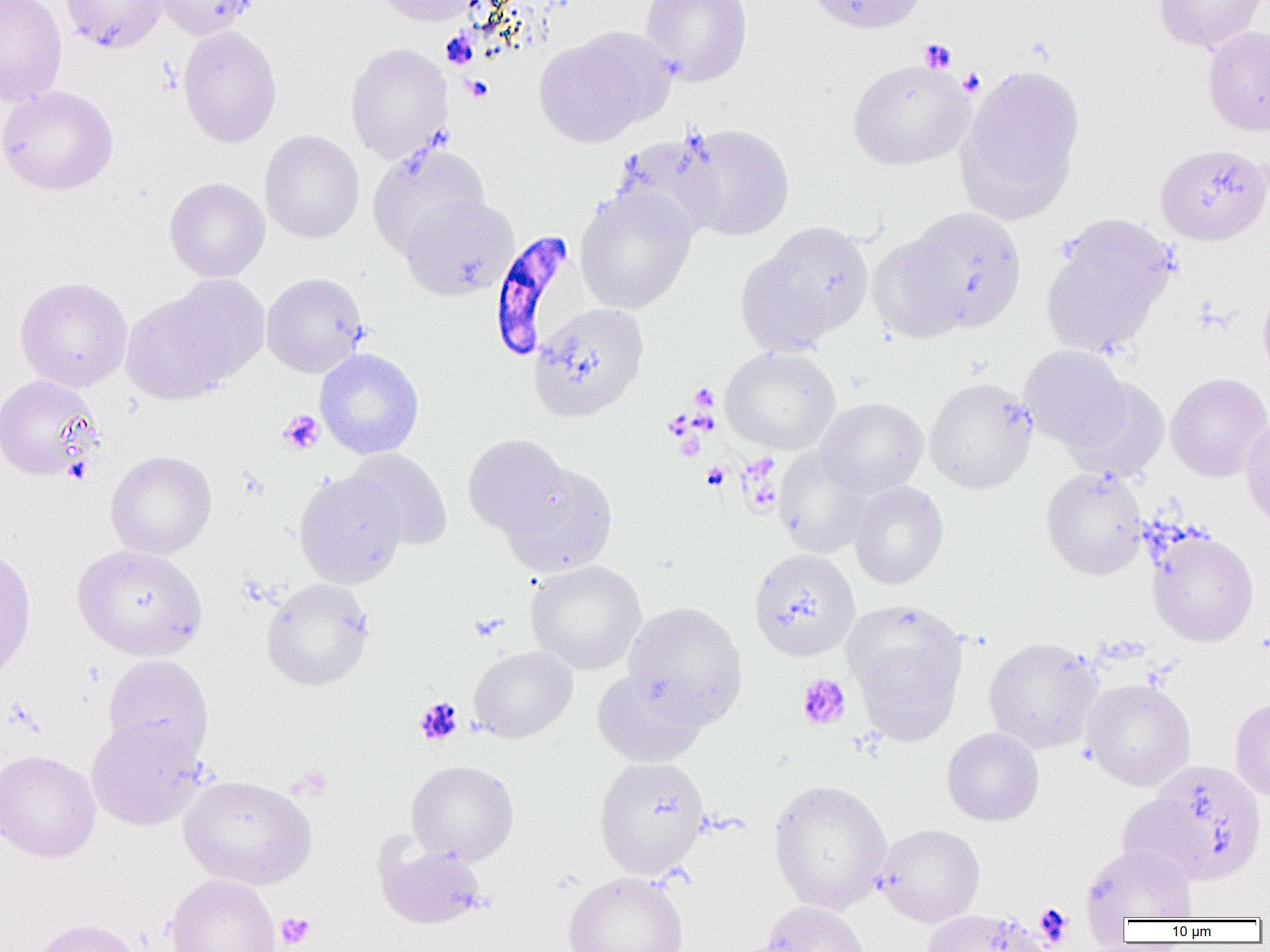
slide-level diagnosis = Plasmodium falciparum
preparation = thin blood film
Plasmodium falciparum-infected red blood cell locations = approximate bounding boxes as [x1, y1, x2, y2] in pixels: [488, 229, 578, 361]
uninfected red blood cell locations = approximate bounding boxes as [x1, y1, x2, y2] in pixels: [0, 0, 67, 107], [61, 0, 167, 53], [153, 0, 258, 40], [372, 0, 484, 26], [641, 0, 753, 86], [803, 0, 930, 34], [1153, 0, 1266, 54], [177, 25, 282, 148], [1202, 26, 1270, 135], [534, 28, 669, 147], [345, 42, 453, 163], [847, 58, 974, 169], [955, 64, 1085, 224], [0, 85, 118, 195], [679, 124, 794, 240], [260, 130, 364, 243], [611, 132, 727, 240], [368, 142, 491, 258], [1155, 143, 1270, 246], [164, 177, 270, 282], [575, 186, 697, 315], [400, 194, 518, 300], [903, 207, 1027, 333], [1040, 215, 1177, 358], [745, 222, 873, 349], [868, 234, 971, 343], [261, 272, 369, 378], [14, 276, 133, 392], [120, 284, 251, 404], [1257, 286, 1270, 383], [528, 302, 649, 421], [1019, 345, 1131, 451], [720, 346, 841, 454], [314, 348, 424, 459], [1165, 372, 1270, 482], [0, 375, 103, 481], [924, 377, 1037, 493], [1064, 379, 1171, 482], [815, 397, 928, 498], [1241, 415, 1270, 530], [463, 434, 571, 538], [774, 447, 876, 557], [346, 448, 453, 550], [105, 451, 217, 559], [499, 461, 618, 577], [1041, 466, 1147, 579], [294, 469, 407, 589], [849, 480, 948, 589], [1147, 530, 1259, 646], [0, 543, 37, 684], [73, 544, 207, 661], [749, 548, 860, 660], [525, 560, 646, 674], [261, 577, 374, 691], [842, 600, 968, 735], [622, 601, 748, 725], [983, 637, 1103, 754], [469, 645, 577, 743], [103, 655, 214, 761], [591, 667, 710, 767], [1081, 678, 1195, 790], [1230, 697, 1270, 803], [85, 716, 209, 830], [942, 727, 1044, 826], [0, 749, 101, 862], [594, 756, 710, 879], [406, 759, 519, 865], [178, 774, 317, 889], [768, 779, 892, 913], [876, 823, 985, 927], [374, 838, 489, 931], [1079, 844, 1198, 923], [563, 871, 689, 952], [164, 874, 281, 952], [758, 900, 871, 952], [921, 908, 1047, 952], [30, 917, 145, 952]
image size = 1270×952 pixels
magnification = 1000x
modality = light microscopy
platelet locations = approximate bounding boxes as [x1, y1, x2, y2] in pixels: [919, 38, 957, 73], [957, 67, 985, 97], [463, 75, 493, 102], [689, 383, 718, 412], [278, 410, 325, 455], [701, 462, 730, 491], [470, 614, 507, 641], [796, 673, 851, 730], [414, 697, 463, 746], [292, 766, 332, 799], [1034, 902, 1073, 947], [275, 912, 315, 949]
field of view = one of a larger specimen